State which parasite is depicted.
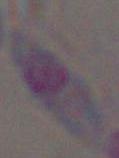

This is Toxoplasma gondii.

Captured at 1000x magnification. Micrograph.